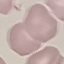
Malaria status: uninfected. Giemsa-stained preparation. Thin smear of blood. Automatically extracted cell patch, resized to 64 × 64 pixels. Photographed with a smartphone camera at the microscope eyepiece.